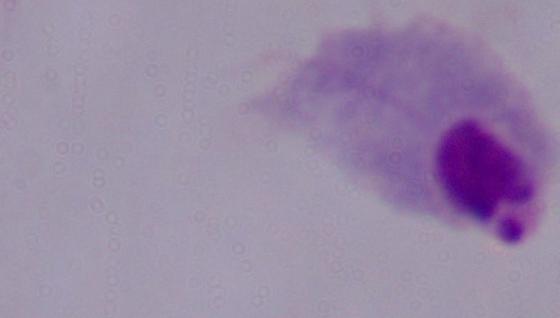
Summary:
  - Modality: micrograph
  - Magnification: 1000x
  - Identification: trichomonad